State the preparation type.
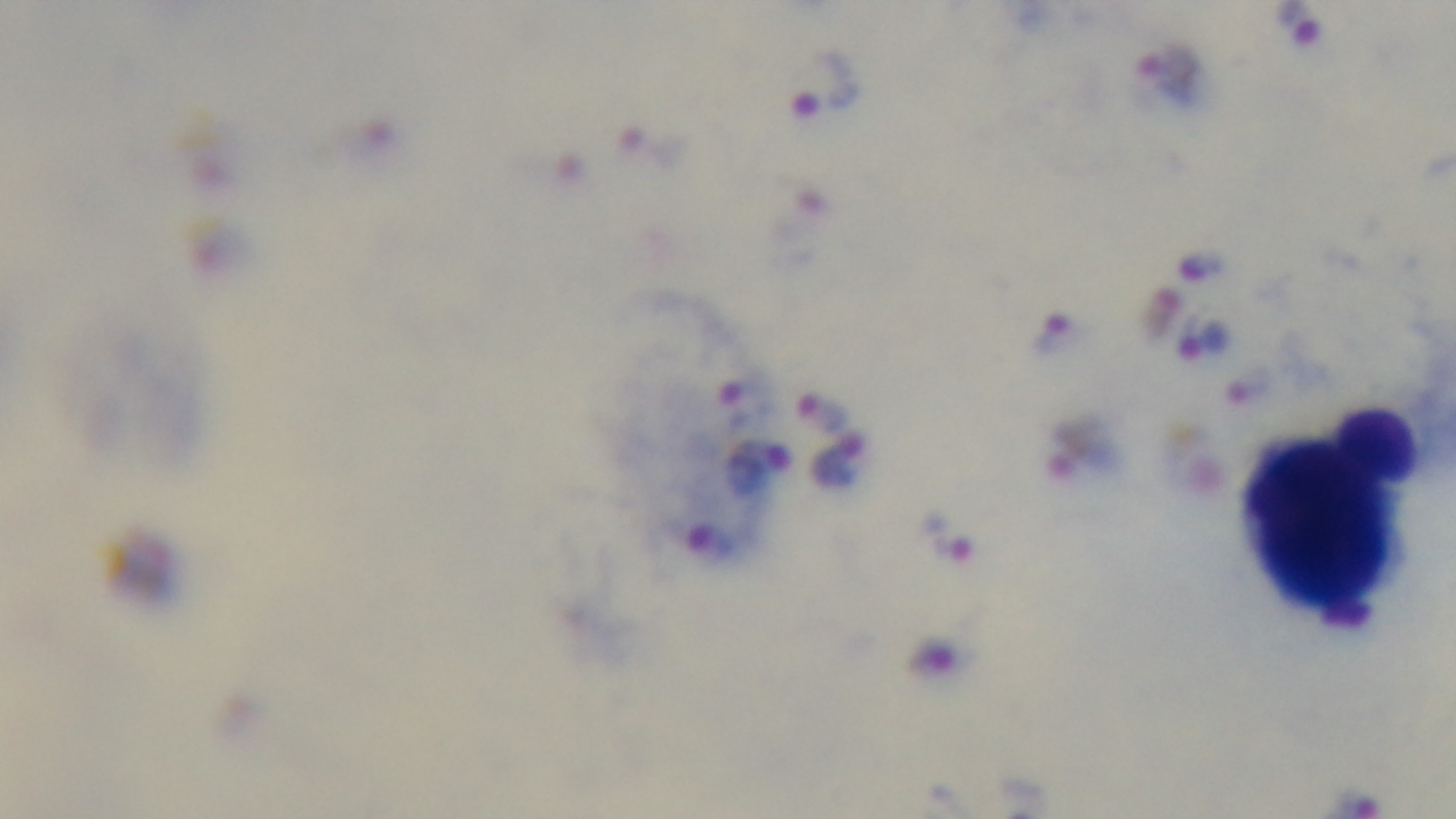

A thick smear.

Summary:
  - Malaria status: positive
  - Capture: mounted 4K digital camera
  - Field of view: single
  - Stain: Giemsa
  - Objective: 100x oil immersion
  - Modality: light microscopy